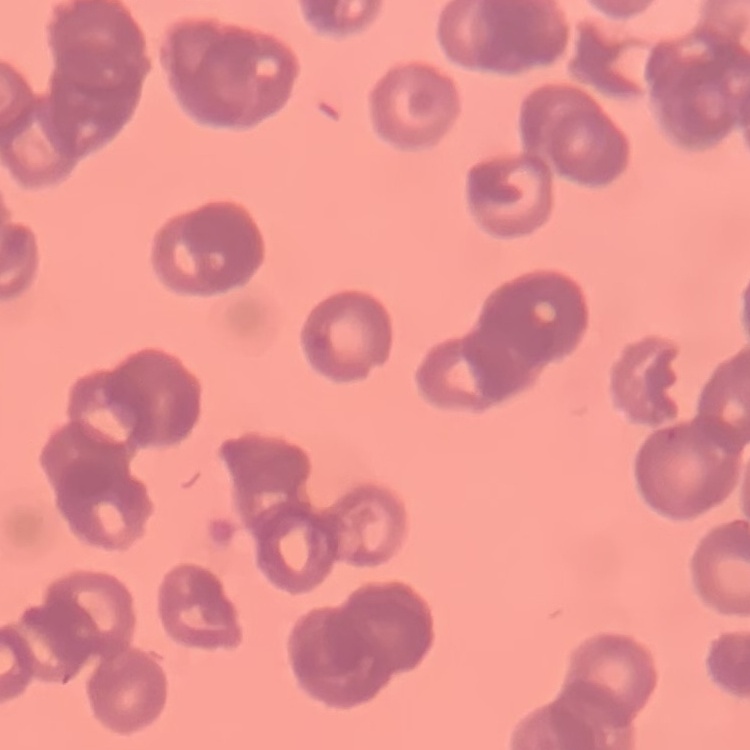

Summary:
  - Erythrocyte morphology: rouleaux formation
  - Image type: square crop of a larger photomicrograph
  - Preparation: thin blood smear
  - Stain: Field's or Giemsa